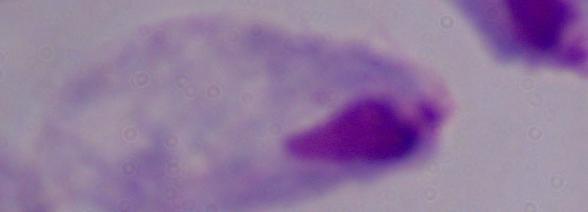 Captured at 1000x magnification. Micrograph. A trichomonad is seen.